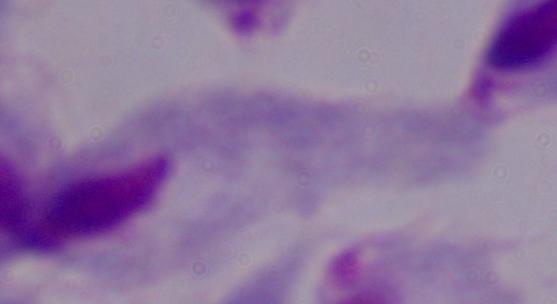

identification = trichomonad
modality = micrograph
magnification = 1000x